Classify this cell by malaria status.
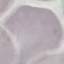

It is uninfected.

Giemsa stain. Cell patch, automatically extracted from a larger field of view and resized to 64 × 64 pixels. Acquired by smartphone through the microscope eyepiece. Thin blood smear.